State which parasite is depicted.
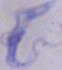

A trypanosome.

magnification = 1000x
modality = photomicrograph